Give the location of every parasitized red blood cell.
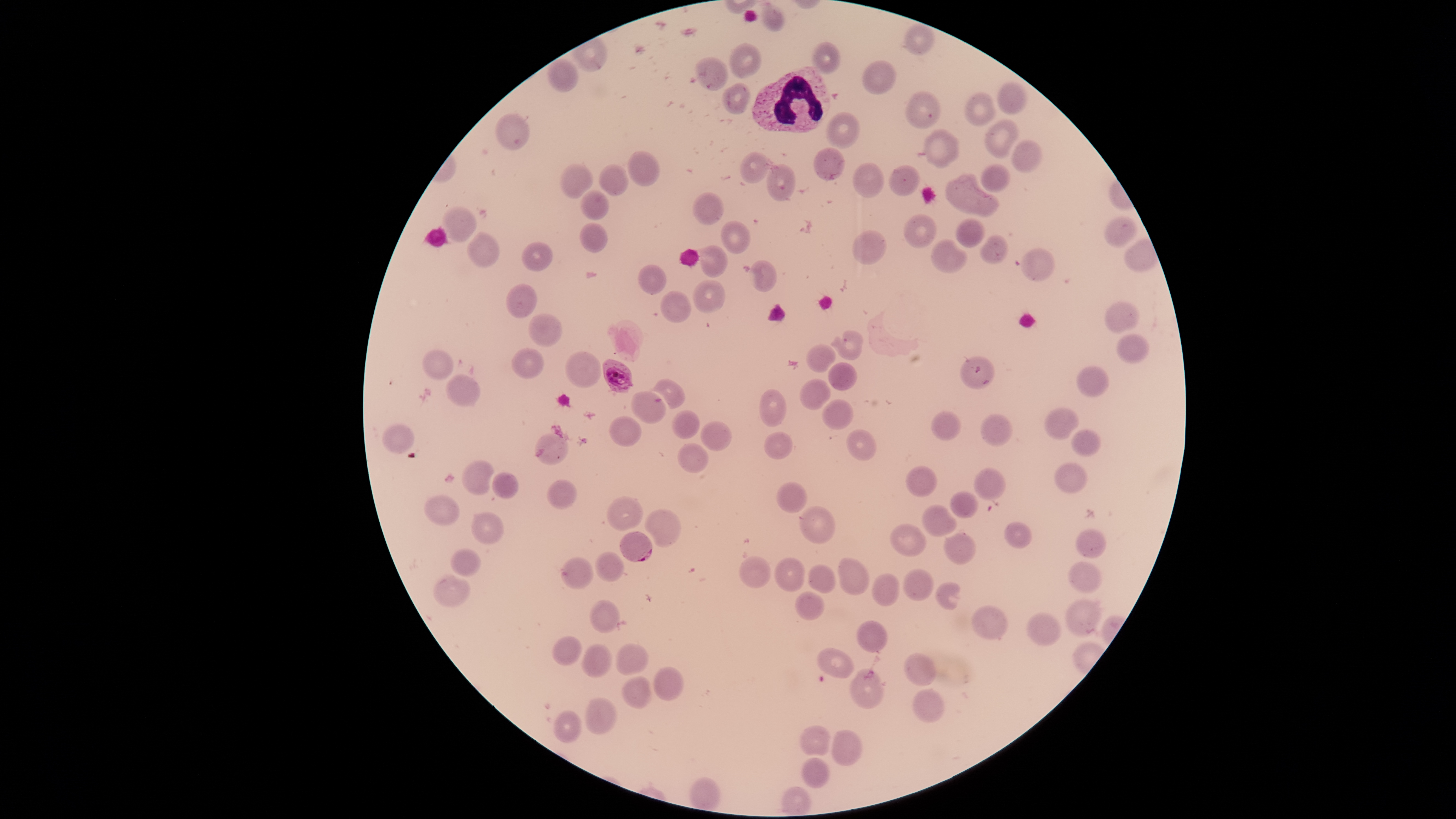

Approximate bounding boxes, in pixels from the top-left corner.
Parasitized red blood cells: (left=602, top=359, right=633, bottom=393), (left=619, top=531, right=653, bottom=562).

Approximate bounding boxes, in pixels from the top-left corner. Uninfected red blood cells: (left=762, top=4, right=784, bottom=32), (left=905, top=24, right=935, bottom=56), (left=729, top=42, right=763, bottom=78), (left=813, top=42, right=841, bottom=74), (left=695, top=57, right=728, bottom=89), (left=863, top=60, right=896, bottom=94), (left=998, top=82, right=1028, bottom=115), (left=723, top=83, right=751, bottom=114), (left=905, top=91, right=941, bottom=128), (left=966, top=92, right=995, bottom=127), (left=497, top=113, right=529, bottom=151), (left=828, top=113, right=858, bottom=150), (left=987, top=118, right=1020, bottom=158), (left=924, top=129, right=960, bottom=169), (left=1011, top=140, right=1042, bottom=173), (left=814, top=147, right=845, bottom=181), (left=740, top=151, right=769, bottom=184), (left=627, top=152, right=660, bottom=186), (left=560, top=163, right=593, bottom=200), (left=852, top=163, right=885, bottom=198), (left=979, top=164, right=1011, bottom=192), (left=601, top=165, right=629, bottom=197), (left=766, top=165, right=795, bottom=202), (left=889, top=165, right=921, bottom=196), (left=945, top=179, right=997, bottom=218), (left=581, top=190, right=609, bottom=220), (left=693, top=193, right=723, bottom=226), (left=440, top=207, right=476, bottom=241), (left=904, top=216, right=937, bottom=248), (left=1105, top=216, right=1139, bottom=248), (left=955, top=219, right=985, bottom=250), (left=721, top=221, right=752, bottom=255), (left=580, top=222, right=608, bottom=253), (left=852, top=230, right=886, bottom=265), (left=467, top=232, right=500, bottom=267), (left=982, top=236, right=1008, bottom=265), (left=931, top=240, right=967, bottom=275), (left=521, top=241, right=553, bottom=272), (left=700, top=245, right=727, bottom=278), (left=1021, top=248, right=1055, bottom=281), (left=749, top=261, right=778, bottom=292), (left=638, top=264, right=668, bottom=296), (left=694, top=281, right=725, bottom=313), (left=506, top=284, right=538, bottom=319), (left=660, top=290, right=692, bottom=323), (left=1106, top=301, right=1140, bottom=334), (left=528, top=314, right=563, bottom=347), (left=835, top=331, right=863, bottom=360), (left=1117, top=333, right=1149, bottom=361), (left=805, top=343, right=835, bottom=373), (left=511, top=348, right=543, bottom=379), (left=422, top=350, right=454, bottom=380), (left=566, top=351, right=602, bottom=388), (left=962, top=357, right=994, bottom=390), (left=828, top=363, right=857, bottom=393), (left=1078, top=365, right=1110, bottom=396), (left=447, top=374, right=480, bottom=406), (left=654, top=379, right=684, bottom=409), (left=799, top=379, right=831, bottom=410), (left=759, top=389, right=785, bottom=428), (left=631, top=390, right=665, bottom=425), (left=823, top=399, right=853, bottom=431), (left=1043, top=407, right=1081, bottom=440), (left=670, top=411, right=700, bottom=439), (left=932, top=411, right=961, bottom=441), (left=981, top=414, right=1012, bottom=446), (left=608, top=415, right=643, bottom=448), (left=701, top=422, right=732, bottom=451), (left=381, top=423, right=414, bottom=455), (left=1072, top=428, right=1101, bottom=457), (left=847, top=429, right=876, bottom=460), (left=535, top=432, right=569, bottom=466), (left=763, top=433, right=794, bottom=460), (left=678, top=443, right=708, bottom=473), (left=462, top=460, right=495, bottom=497), (left=1055, top=461, right=1087, bottom=493), (left=907, top=466, right=938, bottom=498), (left=974, top=469, right=1005, bottom=501), (left=491, top=473, right=518, bottom=498), (left=546, top=480, right=578, bottom=510), (left=778, top=483, right=807, bottom=513), (left=950, top=490, right=978, bottom=519), (left=423, top=495, right=460, bottom=525), (left=607, top=498, right=643, bottom=530), (left=923, top=505, right=955, bottom=538), (left=800, top=507, right=836, bottom=544), (left=647, top=509, right=681, bottom=548), (left=471, top=511, right=504, bottom=544), (left=1004, top=522, right=1033, bottom=550), (left=891, top=524, right=925, bottom=556), (left=1076, top=528, right=1106, bottom=558), (left=944, top=533, right=976, bottom=565), (left=451, top=549, right=481, bottom=577), (left=595, top=552, right=623, bottom=582), (left=739, top=556, right=771, bottom=589), (left=837, top=556, right=870, bottom=595), (left=561, top=557, right=593, bottom=589), (left=776, top=557, right=805, bottom=592), (left=1068, top=563, right=1103, bottom=594), (left=808, top=565, right=836, bottom=594), (left=904, top=568, right=935, bottom=601), (left=433, top=573, right=470, bottom=608), (left=872, top=574, right=900, bottom=607), (left=936, top=581, right=965, bottom=611), (left=796, top=592, right=825, bottom=620), (left=1066, top=599, right=1102, bottom=637), (left=590, top=601, right=620, bottom=633), (left=970, top=605, right=1008, bottom=641), (left=1028, top=613, right=1061, bottom=647), (left=857, top=620, right=887, bottom=653), (left=551, top=636, right=583, bottom=667), (left=582, top=643, right=613, bottom=679), (left=616, top=644, right=649, bottom=674), (left=817, top=649, right=854, bottom=679), (left=903, top=653, right=938, bottom=687), (left=850, top=667, right=885, bottom=708), (left=655, top=668, right=684, bottom=701), (left=621, top=677, right=653, bottom=710), (left=913, top=689, right=944, bottom=723), (left=586, top=698, right=617, bottom=736), (left=554, top=711, right=583, bottom=745), (left=800, top=724, right=833, bottom=757), (left=832, top=730, right=862, bottom=766), (left=802, top=758, right=831, bottom=789). White blood cells: (left=752, top=67, right=831, bottom=132). Giemsa stain. One field of view of the specimen. Species: Plasmodium falciparum. Photographed with a smartphone camera through the microscope eyepiece. Image is 1456×819 pixels. The visible region is circular. Thin blood smear.